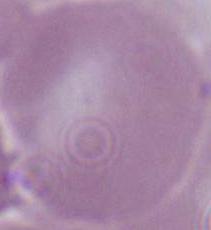
magnification = 1000x
modality = micrograph
identification = erythrocyte